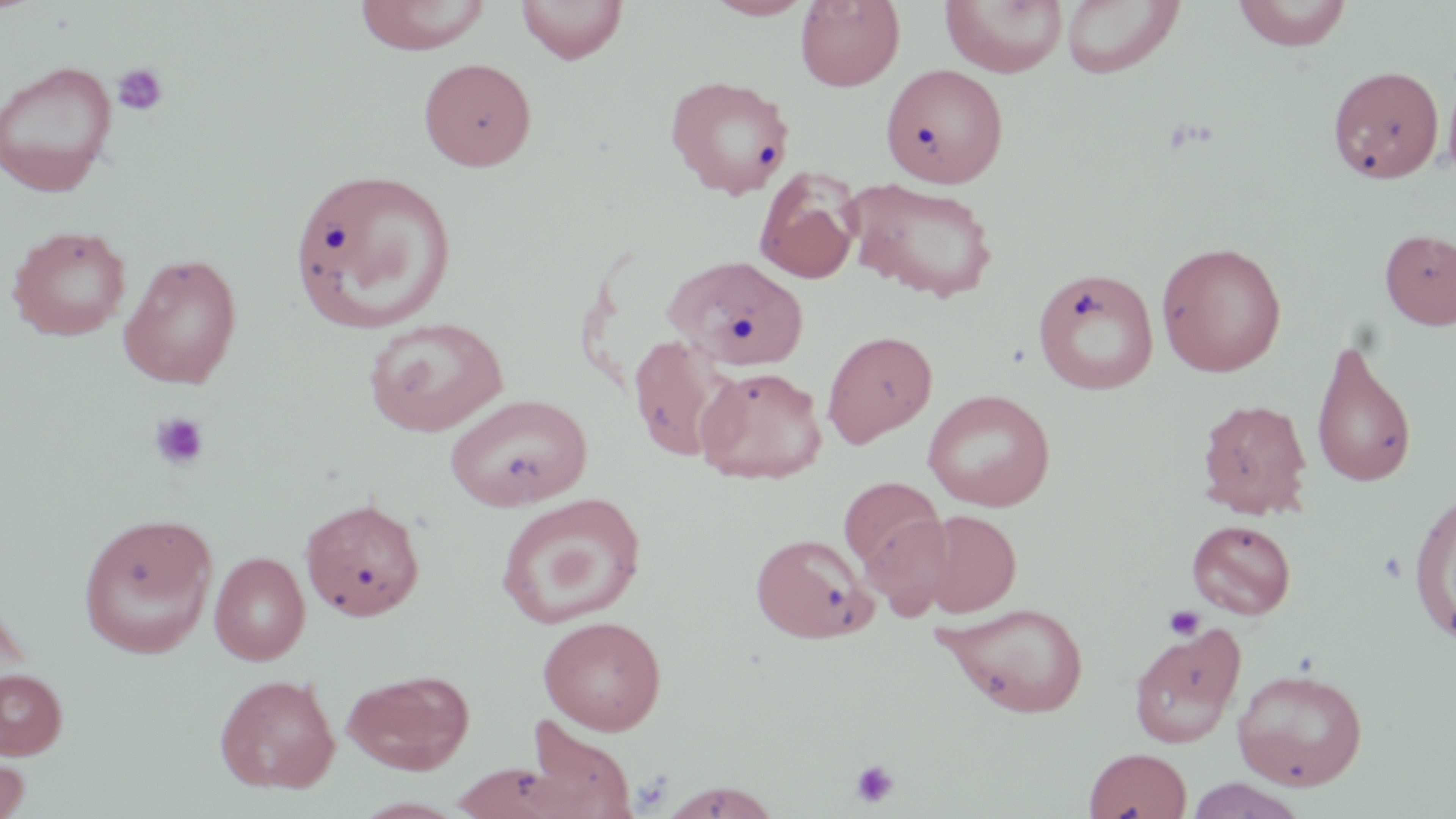

Summary:
  - Coordinate format: approximate bounding boxes as (x1, y1, x2, y2) in pixels
  - Platelet locations: (113, 63, 168, 117), (149, 412, 209, 471), (1162, 604, 1206, 642), (849, 758, 900, 808)
  - Uninfected red blood cell locations: (353, 0, 491, 54), (516, 0, 628, 64), (704, 0, 816, 20), (795, 0, 905, 91), (1060, 0, 1185, 79), (1232, 0, 1353, 50), (940, 1, 1068, 77), (418, 56, 537, 171), (0, 60, 118, 196), (881, 63, 1008, 188), (1328, 64, 1443, 184), (1442, 67, 1456, 184), (665, 75, 794, 199), (288, 166, 459, 334), (755, 169, 861, 284), (844, 177, 999, 303), (7, 224, 132, 341), (1379, 228, 1456, 329), (1155, 240, 1288, 377), (118, 252, 242, 389), (666, 254, 809, 372), (1032, 267, 1160, 396), (363, 315, 509, 436), (823, 329, 937, 448), (628, 335, 735, 462), (1310, 336, 1418, 489), (695, 365, 827, 485), (922, 388, 1056, 511), (444, 393, 592, 510), (1196, 398, 1314, 519), (837, 476, 946, 577), (1408, 485, 1456, 644), (494, 492, 647, 628), (300, 496, 426, 620), (919, 509, 1022, 617), (859, 510, 956, 619), (77, 512, 218, 658), (1186, 518, 1296, 619), (750, 532, 876, 643), (209, 551, 310, 665), (209, 552, 315, 792), (936, 601, 1090, 717), (538, 615, 667, 734), (1128, 623, 1246, 748), (0, 667, 68, 759), (1232, 667, 1368, 790), (343, 669, 474, 774), (214, 673, 340, 793), (521, 718, 638, 819), (1082, 746, 1192, 819), (0, 754, 31, 819), (451, 762, 577, 818), (1184, 777, 1306, 818), (660, 780, 782, 819)
  - Slide-level diagnosis: no evidence of blood parasites
  - Stain: May-Grünwald-Giemsa
  - Modality: light microscopy
  - Image size: 1456×819 pixels
  - Magnification: 1000x
  - Field of view: one of a larger specimen
  - Preparation: thin blood smear